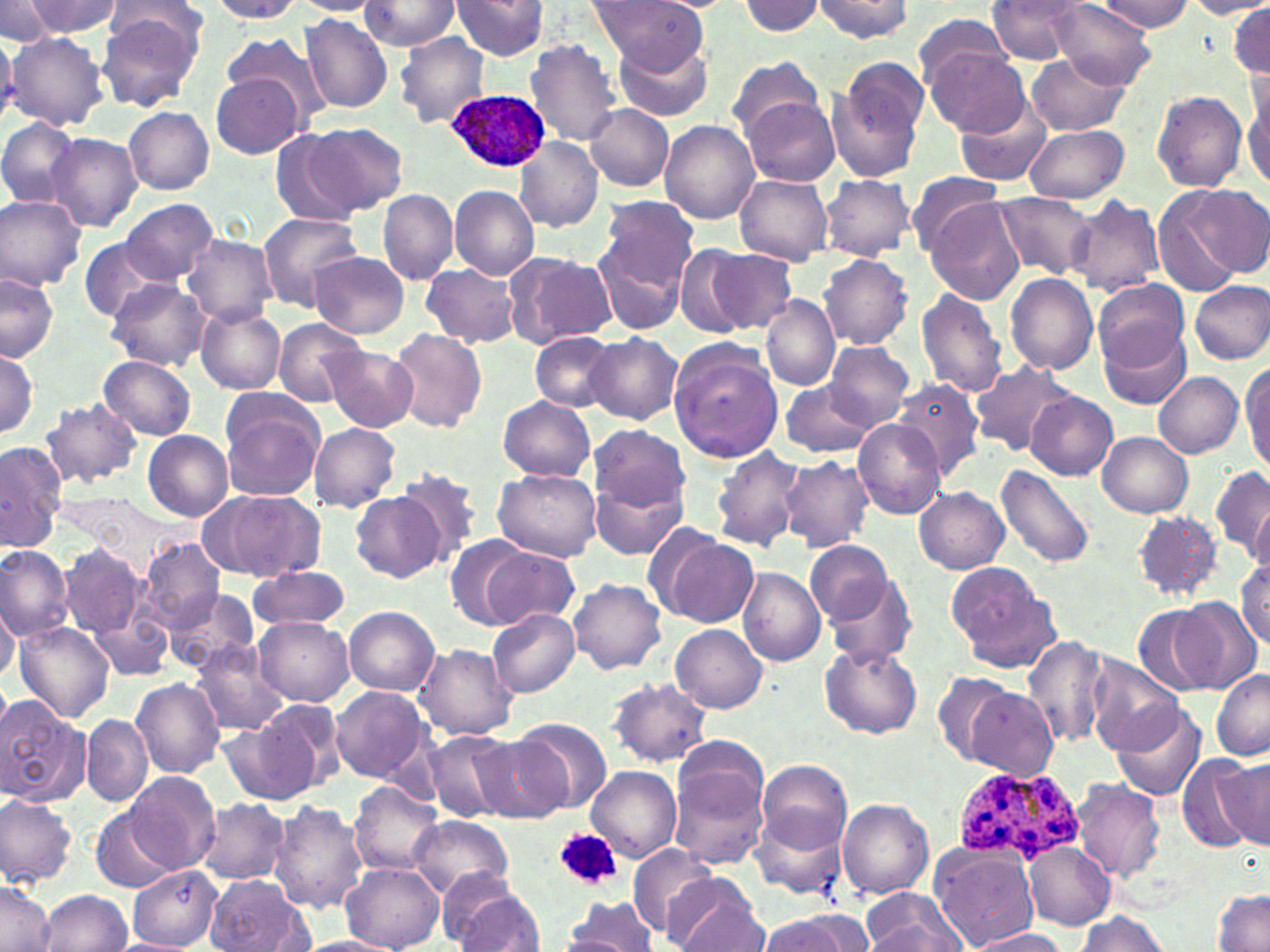

slide_level_diagnosis: Plasmodium ovale
field_of_view: one of a larger specimen
image_size: 1270×952 pixels
magnification: 1000x
plasmodium_ovale_infected_red_blood_cell_locations: 'approximate bounding boxes as (x1, y1, x2, y2) in pixels: (445, 90, 552, 174), (953, 766, 1084, 866)'
modality: optical microscopy
preparation: thin blood smear
platelet_locations: 'approximate bounding boxes as (x1, y1, x2, y2) in pixels: (555, 828, 624, 889)'
uninfected_red_blood_cell_locations: 'approximate bounding boxes as (x1, y1, x2, y2) in pixels: (454, 0, 547, 60), (589, 0, 707, 72), (812, 0, 915, 42), (986, 0, 1087, 62), (21, 1, 123, 37), (208, 1, 304, 23), (291, 1, 386, 15), (360, 1, 460, 50), (736, 1, 826, 37), (1096, 1, 1193, 31), (1186, 1, 1270, 19), (0, 2, 60, 45), (104, 2, 208, 56), (1051, 3, 1154, 87), (1226, 6, 1270, 77), (97, 11, 201, 112), (913, 13, 1012, 91), (300, 14, 391, 114), (7, 30, 109, 130), (220, 33, 328, 121), (396, 33, 489, 130), (0, 35, 22, 121), (616, 37, 715, 122), (524, 39, 624, 147), (927, 48, 1030, 137), (1026, 55, 1130, 135), (727, 56, 824, 141), (830, 57, 927, 180), (1245, 73, 1270, 192), (211, 74, 305, 159), (1152, 91, 1247, 191), (743, 96, 841, 186), (953, 96, 1052, 187), (585, 105, 673, 191), (123, 108, 214, 195), (0, 115, 82, 208), (659, 119, 760, 224), (302, 122, 408, 215), (1026, 124, 1129, 203), (269, 129, 364, 226), (45, 133, 142, 232), (515, 138, 604, 232), (735, 171, 833, 266), (905, 173, 1008, 255), (820, 175, 915, 260), (450, 185, 540, 279), (1183, 185, 1269, 277), (378, 189, 457, 283), (1152, 190, 1245, 296), (994, 192, 1095, 279), (0, 193, 87, 291), (1068, 195, 1164, 298), (593, 197, 700, 324), (121, 199, 218, 285), (927, 200, 1025, 305), (256, 211, 364, 309), (182, 236, 276, 325), (79, 238, 166, 322), (674, 244, 753, 338), (707, 249, 797, 333), (309, 251, 409, 338), (507, 252, 618, 348), (820, 254, 912, 350), (423, 263, 519, 348), (1005, 273, 1099, 375), (0, 274, 59, 362), (104, 278, 210, 372), (1092, 280, 1189, 371), (1188, 280, 1270, 365), (915, 287, 1009, 399), (761, 295, 840, 390), (196, 305, 286, 394), (272, 317, 367, 407), (1097, 320, 1191, 408), (387, 328, 486, 433), (531, 332, 619, 413), (587, 334, 681, 424), (824, 341, 915, 428), (668, 343, 782, 462), (325, 346, 418, 431), (0, 349, 39, 436), (99, 356, 197, 439), (970, 359, 1076, 457), (1241, 361, 1270, 473), (1153, 372, 1243, 459), (892, 378, 983, 481), (779, 380, 874, 458), (1027, 393, 1116, 480), (219, 396, 327, 499), (497, 396, 595, 482), (38, 399, 143, 491), (852, 418, 947, 519), (308, 423, 401, 512), (588, 424, 689, 513), (142, 430, 233, 521), (1097, 432, 1193, 518), (1, 440, 64, 552), (710, 445, 803, 551), (779, 457, 873, 553), (995, 463, 1097, 570), (1211, 466, 1270, 560), (491, 467, 603, 562), (394, 468, 484, 565), (588, 473, 687, 562), (914, 487, 1009, 574), (200, 488, 326, 582), (351, 491, 447, 582), (1248, 497, 1270, 582), (1133, 511, 1224, 602), (655, 533, 759, 629), (445, 536, 535, 628), (137, 538, 225, 632), (806, 542, 894, 629), (61, 545, 145, 641), (0, 546, 74, 642), (482, 547, 581, 632), (1235, 557, 1269, 651), (245, 565, 351, 630), (737, 567, 827, 665), (946, 568, 1055, 668), (821, 569, 918, 666), (568, 578, 666, 676), (164, 590, 261, 676), (89, 597, 175, 686), (1170, 598, 1262, 692), (0, 601, 20, 684), (1134, 605, 1222, 697), (345, 606, 440, 694), (487, 608, 580, 697), (253, 617, 355, 706), (14, 621, 116, 722), (672, 624, 767, 713), (1022, 635, 1110, 751), (190, 642, 290, 734), (416, 644, 519, 739), (820, 644, 921, 738), (1086, 656, 1184, 754), (1212, 671, 1270, 761), (930, 674, 1016, 765), (130, 678, 224, 778), (608, 678, 712, 767), (330, 686, 430, 783), (966, 688, 1057, 778), (1, 695, 90, 807), (246, 698, 347, 799), (1110, 702, 1204, 803), (82, 713, 151, 806), (216, 717, 316, 806), (515, 718, 612, 814), (424, 729, 515, 823), (474, 732, 573, 824), (1215, 755, 1270, 851), (757, 759, 851, 856), (671, 761, 773, 870), (586, 765, 682, 863), (125, 771, 219, 873), (1072, 778, 1166, 885), (350, 780, 442, 875), (0, 793, 78, 886), (269, 798, 373, 913), (196, 799, 289, 883), (838, 799, 933, 898), (752, 805, 849, 900), (92, 810, 174, 892), (407, 816, 514, 900), (1023, 840, 1115, 929), (931, 844, 1039, 951), (628, 845, 720, 937), (342, 864, 443, 950), (129, 867, 223, 947), (665, 872, 765, 951), (203, 874, 312, 951), (440, 874, 544, 952), (0, 884, 57, 951), (860, 889, 966, 952), (39, 890, 132, 952), (1212, 890, 1270, 950), (559, 897, 661, 950), (1074, 911, 1173, 951), (755, 913, 872, 952), (970, 928, 1072, 952), (546, 934, 656, 950), (292, 936, 402, 951)'
stain: May-Grünwald-Giemsa